Outline each blood parasite and name the species.
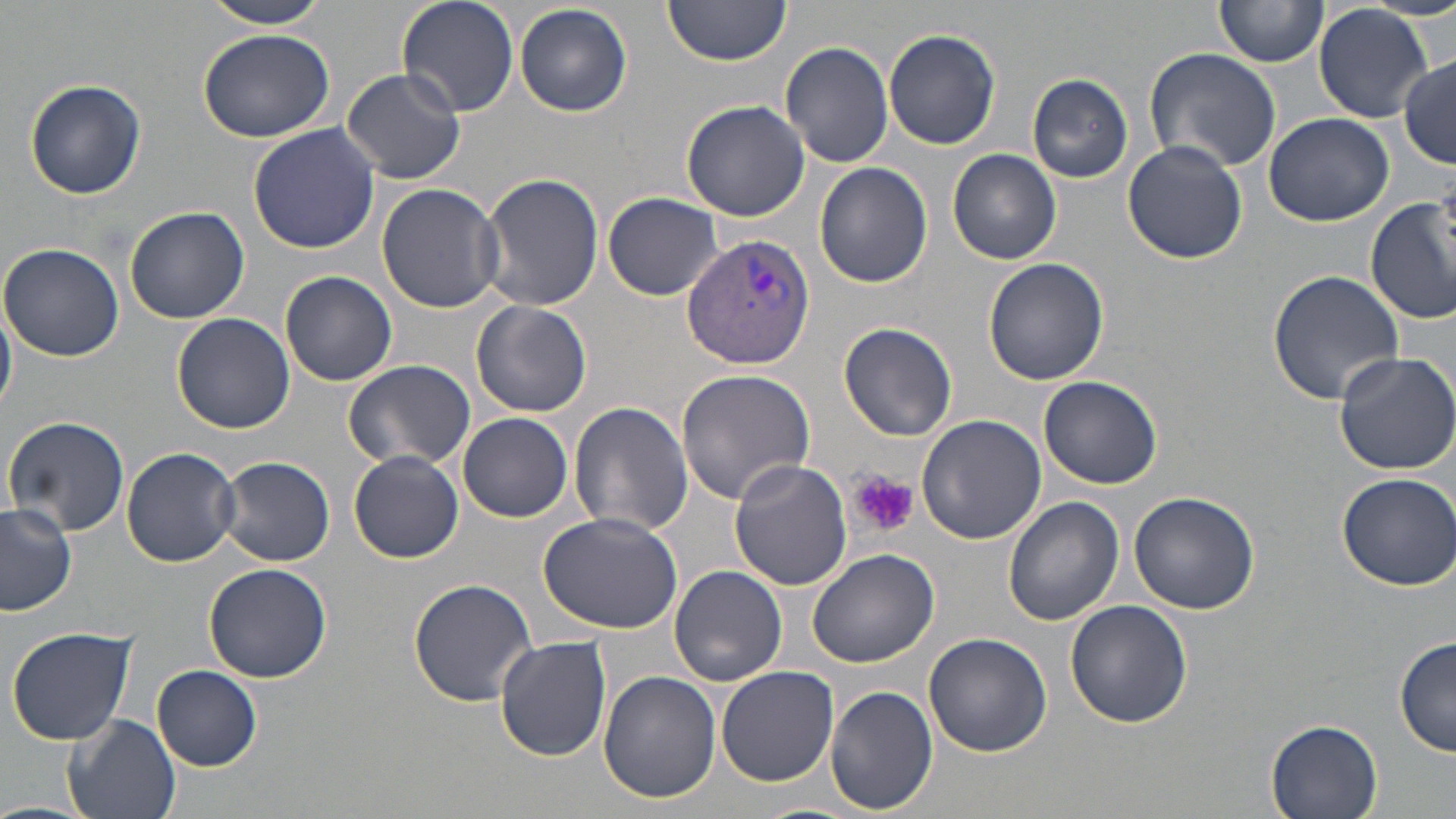
Approximate bounding boxes as [x1, y1, x2, y2] in pixels.
Plasmodium vivax-infected red blood cells: [682, 233, 814, 369].
No Plasmodium falciparum, Plasmodium ovale, Plasmodium malariae, Babesia divergens, or Trypanosoma brucei observed.

slide-level diagnosis = Plasmodium vivax
preparation = thin blood smear
stain = May-Grünwald-Giemsa
image size = 1456×819 pixels
platelet locations = approximate bounding boxes as [x1, y1, x2, y2] in pixels: [851, 472, 917, 537]
uninfected red blood cell locations = approximate bounding boxes as [x1, y1, x2, y2] in pixels: [200, 0, 336, 28], [396, 0, 519, 118], [659, 0, 789, 68], [1215, 0, 1327, 69], [515, 3, 632, 116], [1315, 5, 1432, 122], [195, 25, 335, 144], [883, 28, 1001, 150], [780, 40, 894, 170], [1142, 46, 1281, 175], [1398, 54, 1456, 168], [340, 67, 467, 186], [1028, 73, 1134, 183], [23, 78, 149, 199], [681, 99, 809, 222], [1264, 112, 1393, 227], [247, 123, 379, 254], [1123, 140, 1250, 263], [948, 148, 1062, 264], [813, 162, 932, 289], [479, 170, 604, 312], [377, 183, 510, 313], [603, 192, 725, 301], [1367, 192, 1456, 325], [124, 205, 251, 324], [0, 244, 126, 362], [983, 259, 1110, 387], [1267, 269, 1404, 403], [280, 270, 397, 386], [0, 296, 16, 420], [470, 301, 592, 418], [172, 313, 295, 434], [841, 322, 957, 442], [1330, 349, 1456, 476], [342, 359, 476, 472], [677, 368, 816, 506], [1039, 375, 1166, 490], [569, 400, 695, 540], [916, 412, 1046, 547], [459, 413, 573, 522], [2, 415, 131, 538], [122, 446, 240, 568], [349, 450, 464, 563], [217, 455, 335, 567], [727, 460, 853, 591], [1335, 471, 1456, 591], [1127, 488, 1260, 613], [1002, 497, 1123, 627], [0, 504, 76, 618], [538, 511, 683, 636], [805, 547, 940, 667], [203, 563, 332, 682], [668, 565, 787, 685], [408, 577, 538, 707], [1064, 599, 1193, 728], [6, 626, 137, 746], [923, 632, 1053, 758], [1395, 634, 1455, 758], [494, 638, 611, 762], [715, 664, 839, 788], [151, 665, 261, 770], [599, 671, 721, 806], [824, 684, 939, 814], [62, 713, 181, 819], [1264, 719, 1383, 819], [0, 800, 93, 819]
field of view = one of a larger specimen
magnification = 1000x
modality = optical microscopy